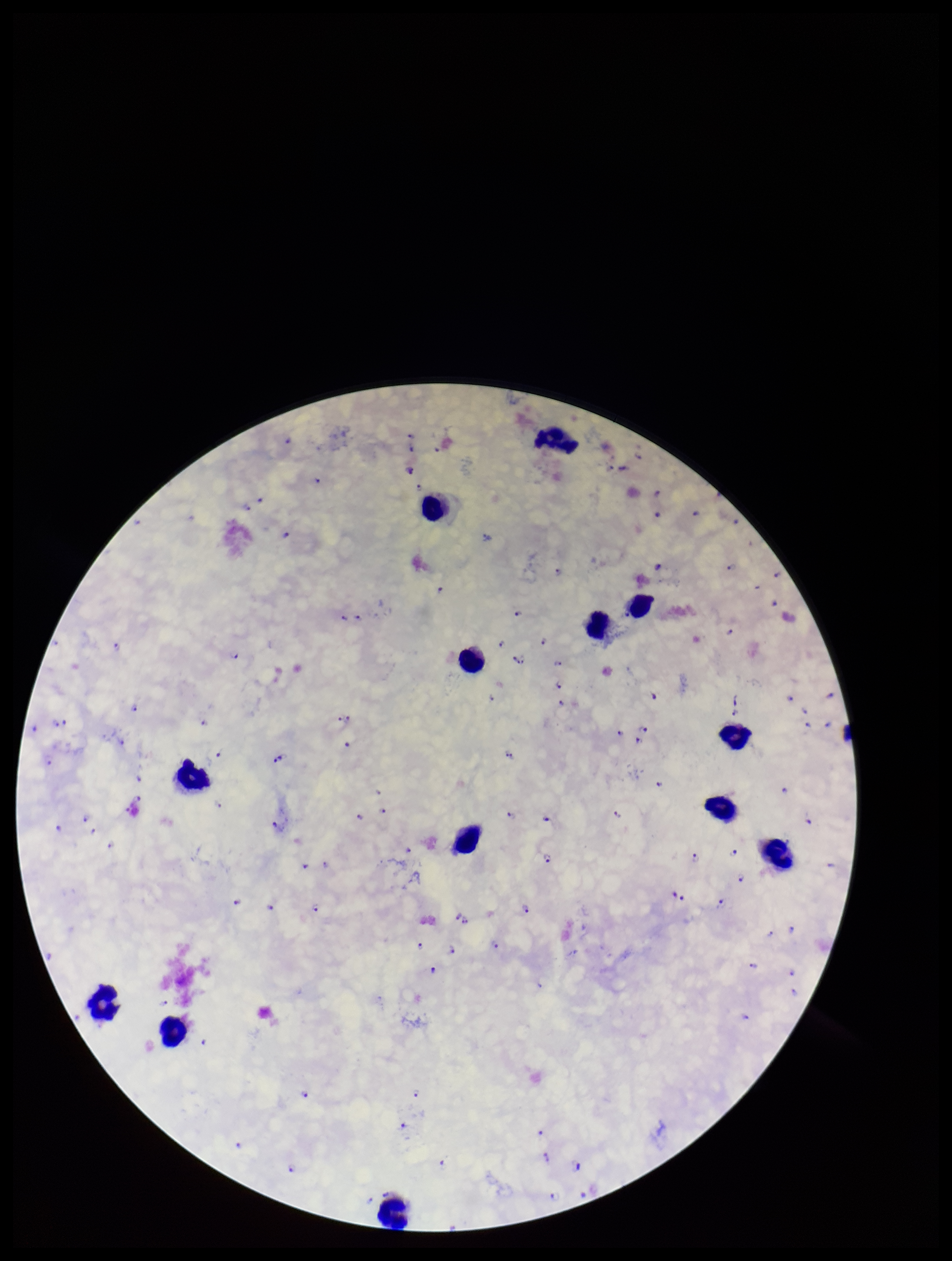
Preparation: thick. Smartphone photograph taken through the eyepiece of a microscope. Plasmodium parasites: seen. Single field of view. Stained with Giemsa. Species reported for this patient: Plasmodium falciparum. Parasite count: 105. Image is 952×1261 pixels. Patient malaria status: infected. Leukocyte count: 12.